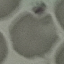
Summary:
  - Result: no malaria parasites detected
  - Capture: smartphone camera at the microscope eyepiece
  - Image type: cell patch, automatically extracted from a larger field of view and resized to 64 × 64 pixels
  - Preparation: thin smear
  - Stain: Giemsa